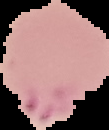

Result: Plasmodium parasites identified. Image is 109×130 pixels. From a thin blood smear. Segmented cell region on a black background.